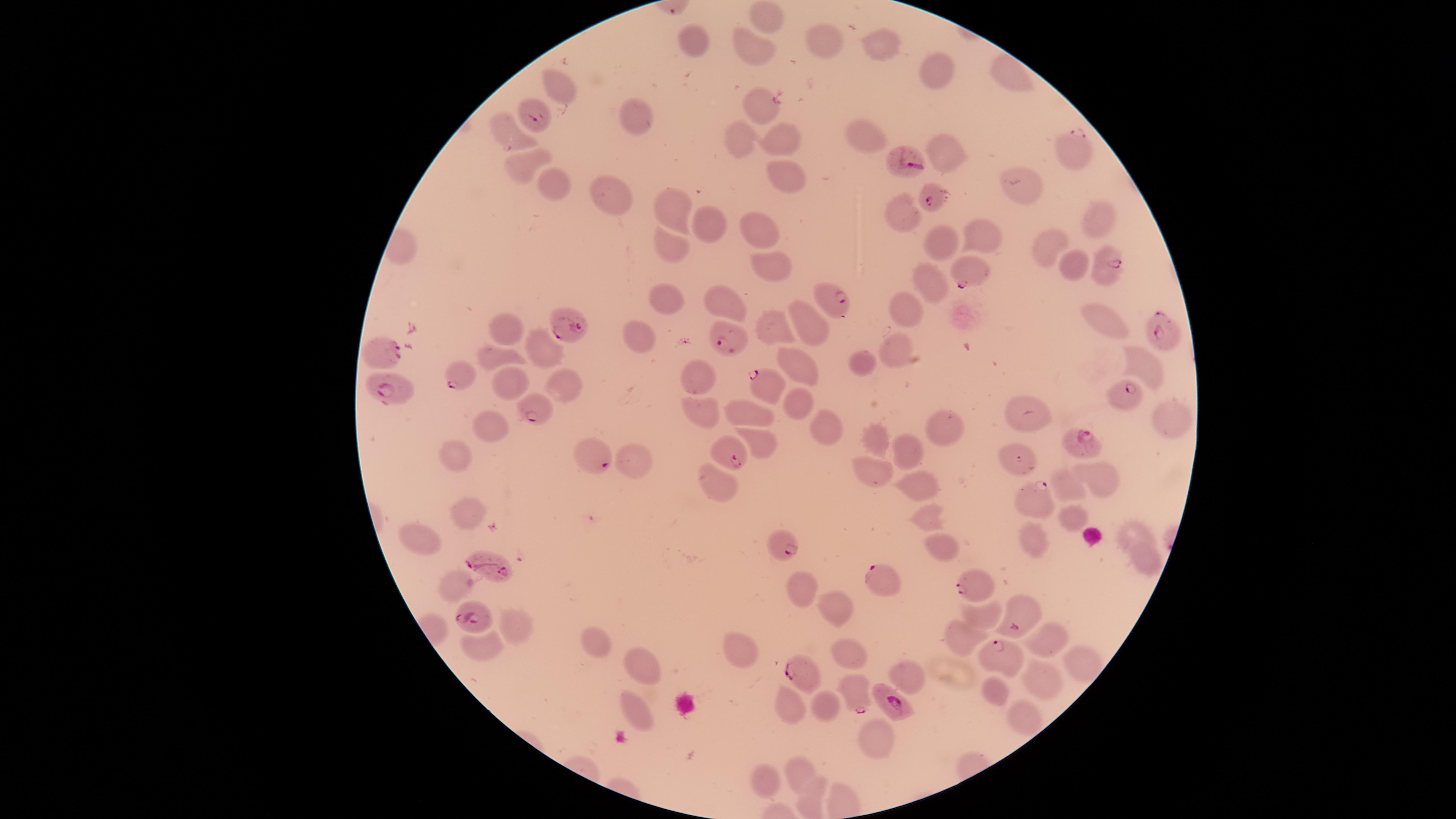
capture: smartphone photograph through the microscope eyepiece
field_of_view: single
parasitized_RBCs: 'approximate marker points as {x, y} in pixels: {538, 117}, {1076, 150}, {911, 157}, {931, 195}, {1106, 264}, {968, 268}, {830, 296}, {569, 326}, {1161, 331}, {730, 335}, {385, 350}, {460, 375}, {767, 383}, {390, 388}, {1126, 394}, {532, 413}, {1078, 442}, {591, 451}, {729, 456}, {1032, 498}, {784, 545}, {488, 565}, {882, 579}, {970, 584}, {474, 616}, {1016, 623}, {1001, 655}, {799, 672}, {854, 690}, {891, 700}'
image_size: 1456×819 pixels
visible_region: circular
presence: malaria parasites detected
preparation: thin blood smear
uninfected_RBCs: 'approximate marker points as {x, y} in pixels: {766, 16}, {818, 37}, {699, 38}, {879, 41}, {749, 46}, {937, 72}, {1012, 74}, {556, 87}, {760, 104}, {637, 112}, {739, 134}, {787, 134}, {508, 136}, {868, 139}, {945, 152}, {519, 159}, {781, 169}, {550, 177}, {1017, 184}, {615, 198}, {676, 201}, {902, 214}, {707, 217}, {1098, 218}, {758, 225}, {980, 231}, {945, 237}, {673, 245}, {1047, 245}, {1072, 260}, {765, 266}, {930, 274}, {670, 299}, {722, 301}, {902, 310}, {809, 321}, {1104, 323}, {511, 327}, {773, 327}, {642, 332}, {545, 344}, {897, 349}, {498, 353}, {799, 361}, {861, 362}, {1136, 363}, {692, 380}, {505, 382}, {558, 387}, {798, 400}, {1024, 407}, {700, 410}, {749, 412}, {1163, 418}, {947, 423}, {487, 425}, {827, 426}, {868, 439}, {757, 445}, {905, 448}, {1016, 452}, {452, 456}, {635, 460}, {863, 469}, {1104, 478}, {721, 482}, {910, 483}, {1064, 486}, {923, 513}, {1072, 514}, {466, 519}, {420, 531}, {1133, 535}, {1033, 538}, {937, 539}, {1144, 561}, {453, 585}, {803, 587}, {835, 606}, {977, 618}, {515, 627}, {1049, 637}, {958, 638}, {592, 639}, {480, 643}, {744, 651}, {1076, 657}, {851, 658}, {641, 659}, {905, 671}, {1036, 678}, {993, 690}, {790, 697}, {821, 708}, {634, 713}, {1020, 715}, {866, 738}, {797, 765}, {763, 780}, {809, 797}'
species: Plasmodium falciparum
stain: Giemsa